State the blood parasite species.
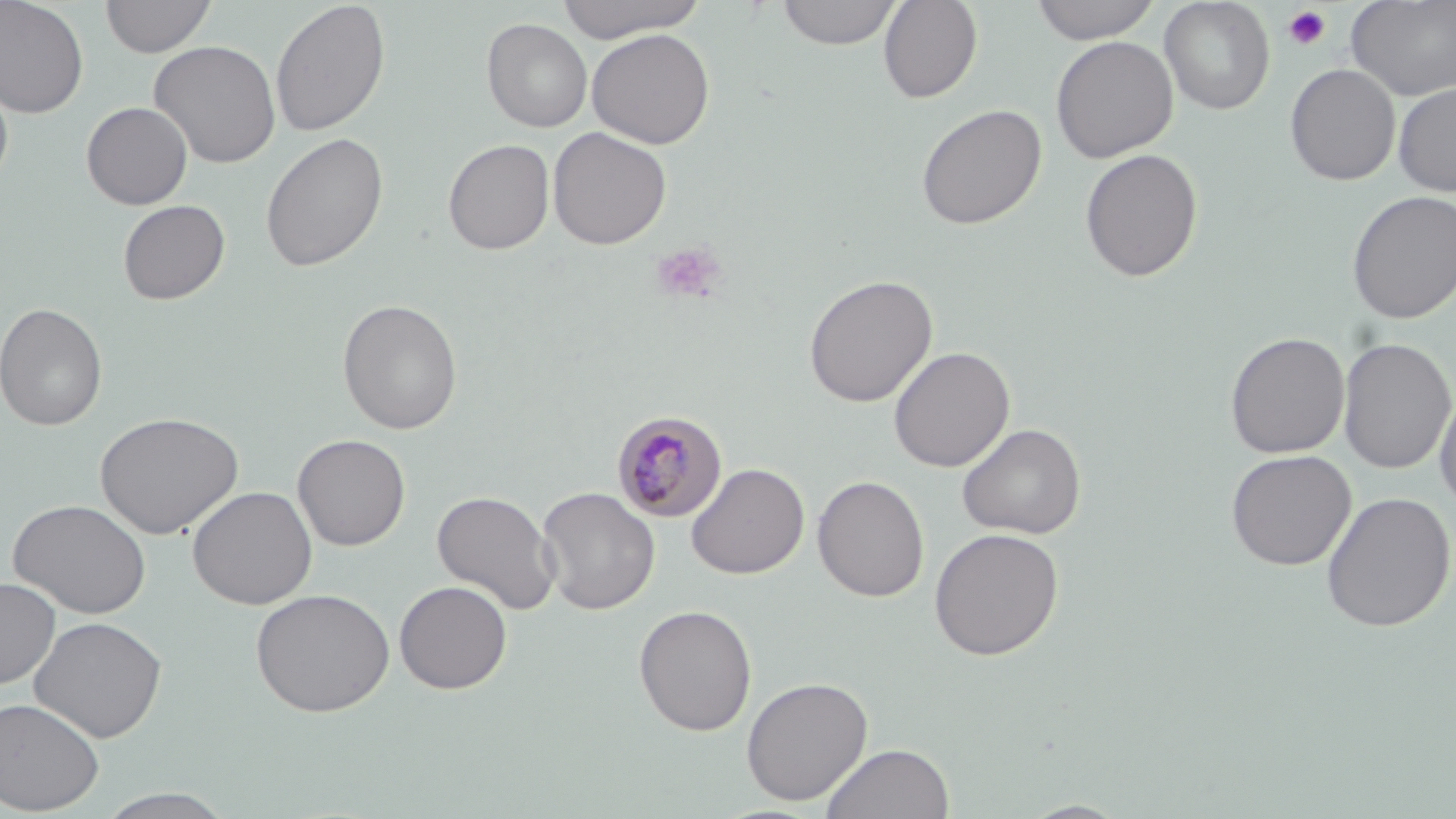

Plasmodium malariae.

Summary:
  - Coordinate format: approximate bounding boxes as (x1, y1, x2, y2) in pixels
  - Uninfected red blood cell locations: (0, 0, 89, 119), (100, 0, 216, 58), (270, 0, 391, 137), (553, 0, 710, 42), (776, 0, 903, 49), (878, 0, 983, 103), (1030, 0, 1163, 44), (1159, 0, 1275, 115), (1346, 0, 1456, 101), (481, 18, 593, 133), (587, 28, 715, 149), (1050, 35, 1178, 163), (148, 40, 281, 169), (1285, 63, 1400, 186), (0, 71, 14, 191), (1393, 82, 1456, 196), (81, 101, 193, 209), (915, 104, 1047, 230), (547, 127, 672, 249), (260, 132, 388, 272), (442, 138, 555, 254), (1080, 148, 1203, 282), (1346, 190, 1456, 324), (117, 199, 230, 305), (803, 274, 938, 407), (337, 299, 463, 434), (0, 302, 108, 432), (1225, 331, 1350, 459), (1337, 337, 1455, 474), (889, 346, 1015, 472), (1434, 386, 1456, 514), (94, 411, 243, 539), (957, 422, 1086, 539), (292, 433, 411, 551), (1225, 449, 1357, 571), (686, 462, 810, 580), (812, 475, 929, 601), (187, 485, 317, 609), (536, 486, 660, 614), (432, 489, 561, 615), (1321, 492, 1455, 632), (7, 498, 152, 619), (928, 527, 1064, 660), (0, 578, 60, 689), (393, 580, 512, 694), (251, 587, 395, 717), (633, 604, 757, 736), (29, 616, 167, 743), (740, 676, 874, 805), (0, 696, 105, 815), (821, 742, 955, 819), (94, 789, 237, 818), (1019, 800, 1131, 818)
  - Platelet locations: (1282, 5, 1332, 50), (649, 241, 727, 304)
  - Plasmodium malariae-infected red blood cell locations: (611, 410, 728, 523)
  - Preparation: thin blood film
  - Field of view: one of a larger specimen
  - Image size: 1456×819 pixels
  - Stain: May-Grünwald-Giemsa
  - Magnification: 1000x
  - Modality: optical microscopy